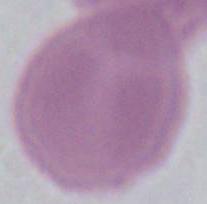

magnification = 1000x
modality = photomicrograph
identification = red blood cell